Comment on the morphology of the erythrocytes.
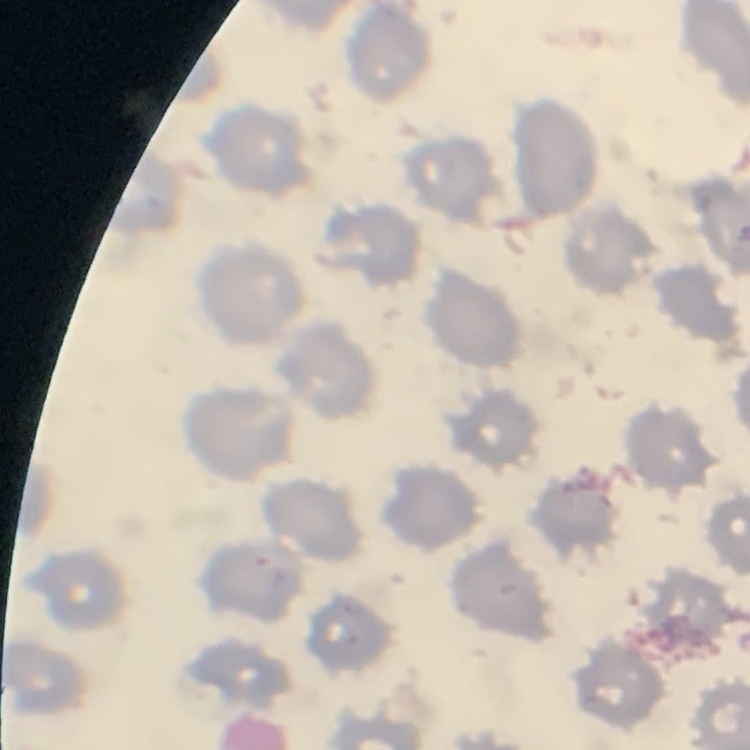
They show no rouleaux formation.

{
  "stain": "Field's or Giemsa",
  "preparation": "thin peripheral smear",
  "image_type": "one tile cut from a larger photomicrograph"
}